Describe the morphology of the erythrocytes.
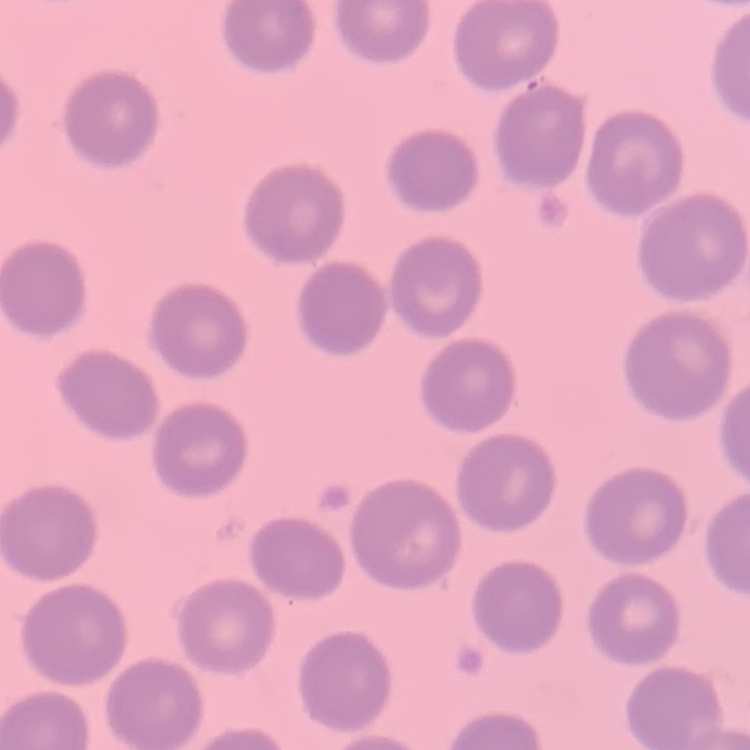

They show no rouleaux formation.

Square crop of a larger photomicrograph. Thin blood film. Stained with either Field's or Giemsa.